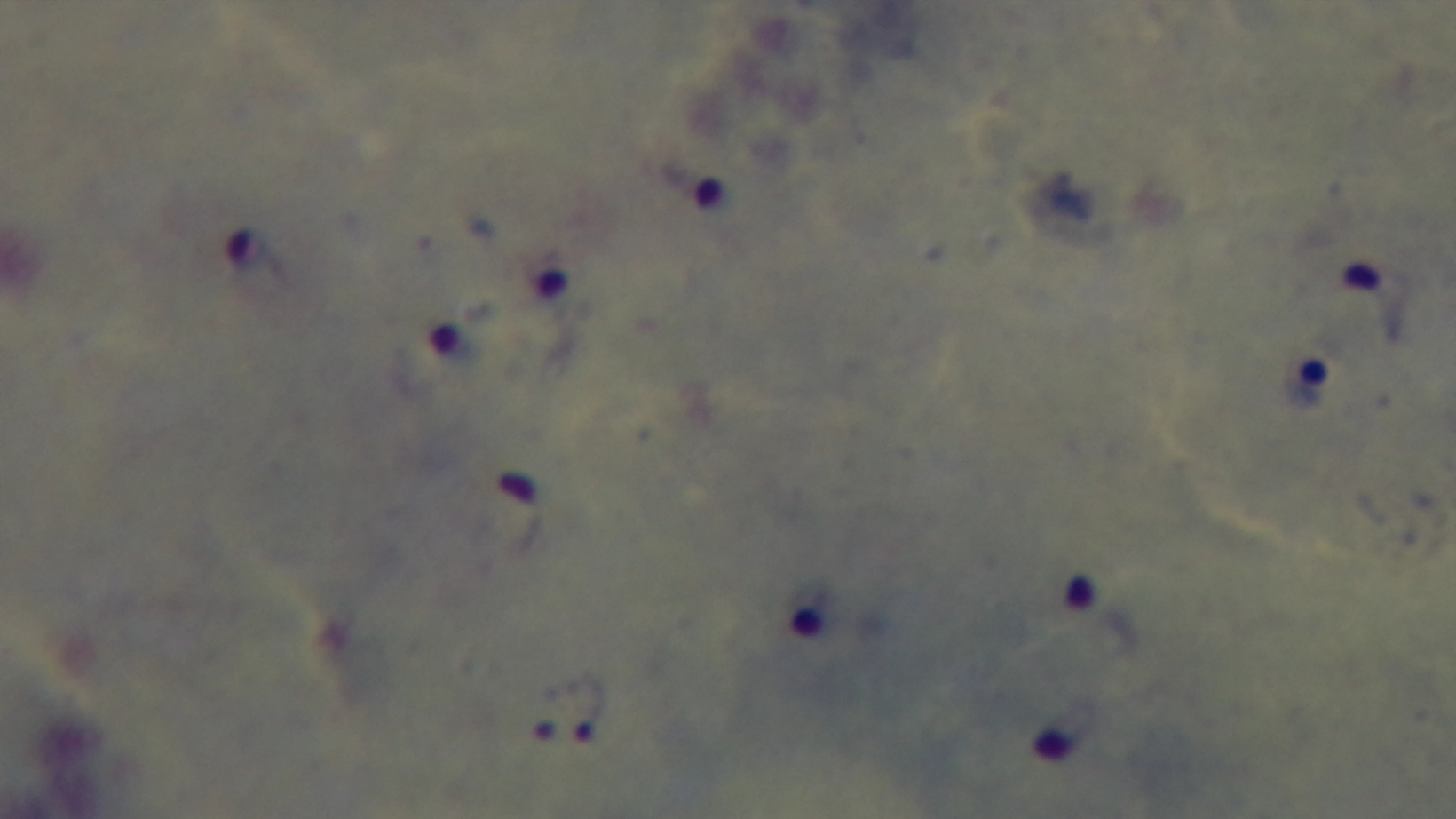
preparation = thick smear
objective = 100x oil immersion
field of view = single
modality = light microscopy
malaria status = positive
capture = mounted 4K digital camera
stain = Giemsa